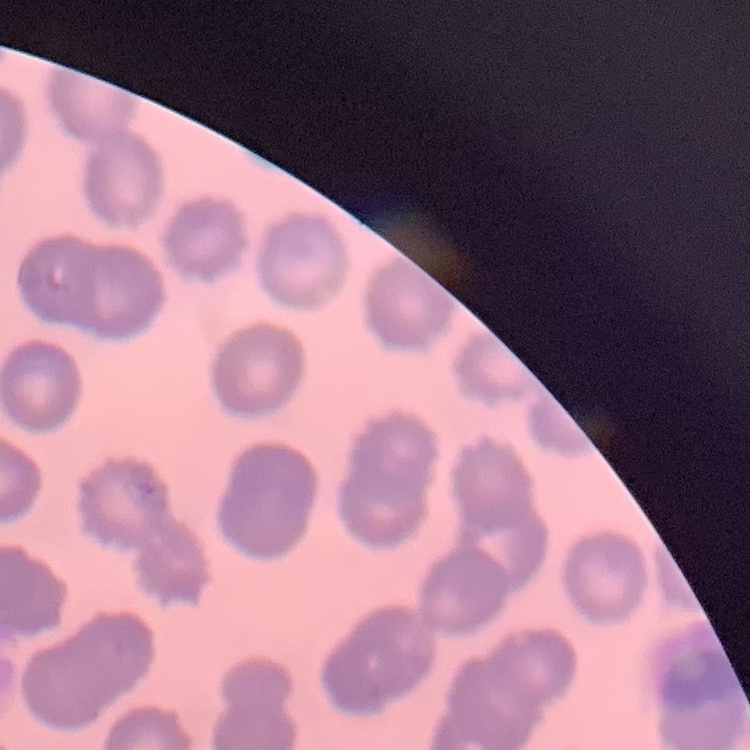
Summary:
  - Erythrocyte morphology: no rouleaux formation
  - Image type: square crop of a larger photomicrograph
  - Preparation: thin blood film
  - Stain: Field's or Giemsa